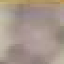
Malaria status: uninfected. Acquired by smartphone through the microscope eyepiece. Giemsa-stained preparation. Thin smear of blood. Cell patch, automatically extracted from a larger field of view and resized to 64 × 64 pixels.